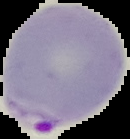

{
  "preparation": "thin blood smear",
  "malaria_status": "parasitized",
  "image_type": "segmented cell region on a black background",
  "image_size": "130×139 pixels"
}